Give the position of every malaria parasite.
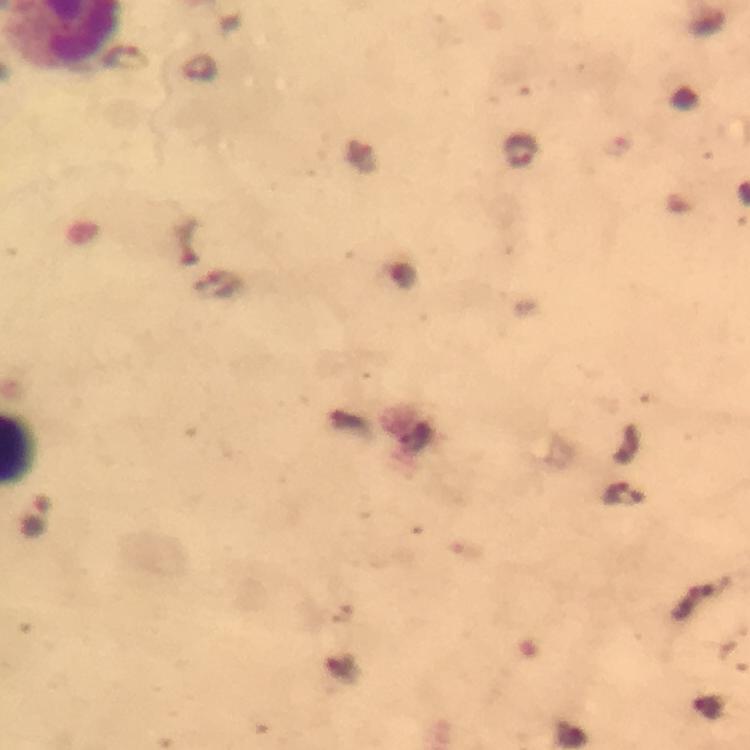
Approximate centers as [x, y] in pixels.
Malaria parasites: [125, 59], [518, 150], [38, 519].

context: from a diagnostic examination for malaria
image_size: 750×750 pixels
preparation: thick smear
immersion_oil: used
cropped_from: a single field of view
capture: smartphone mounted on the microscope
magnification: 100x
stain: Giemsa